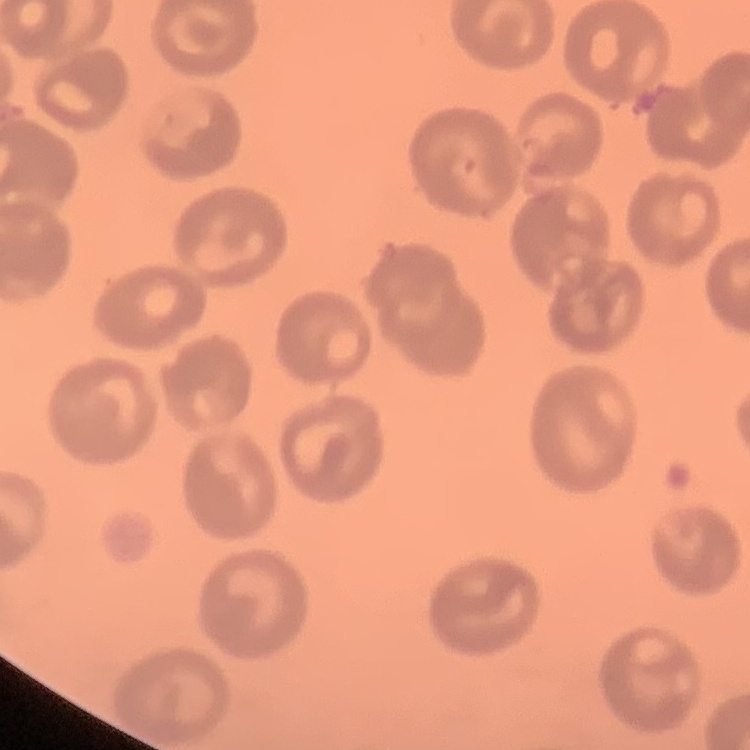

Summary:
  - Erythrocyte morphology: no rouleaux formation
  - Stain: Field's or Giemsa
  - Preparation: thin blood film
  - Image type: square crop of a larger photomicrograph